Classify this cell by malaria status.
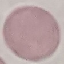
Uninfected.

stain = Giemsa
image type = cell patch, automatically extracted from a larger field of view and resized to 64 × 64 pixels
preparation = thin blood film
capture = smartphone camera at the microscope eyepiece